Classify this cell by malaria status.
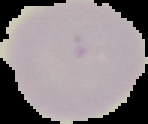
Uninfected.

Summary:
  - Preparation: thin blood smear
  - Image type: segmented cell region with the area outside set to black
  - Image size: 148×124 pixels